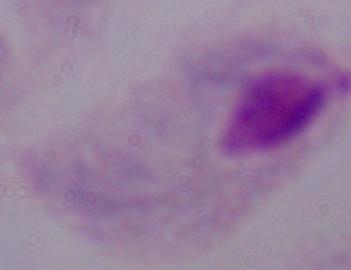

Captured at 1000x magnification. A trichomonad is shown. Micrograph.